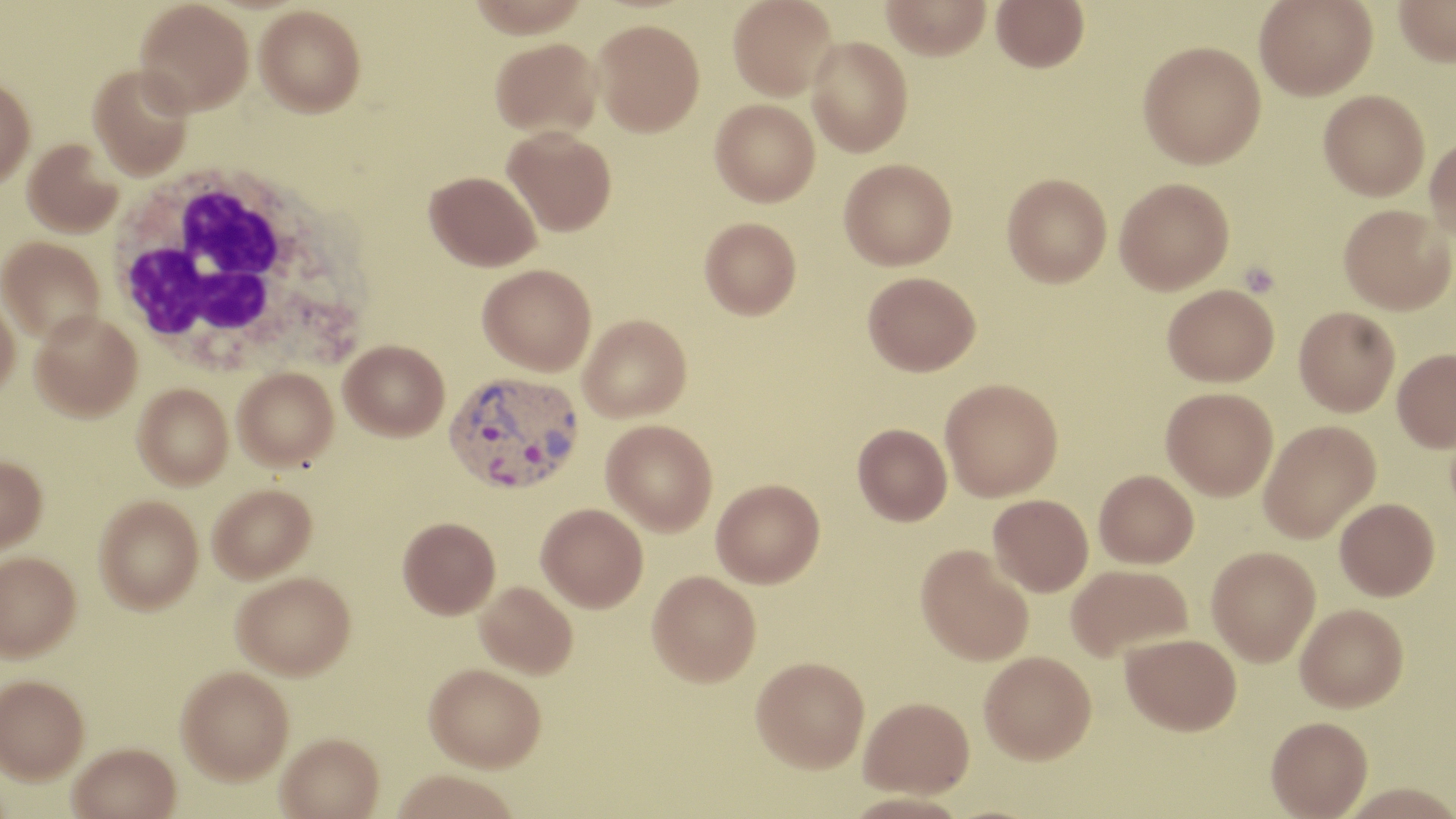
{
  "slide_level_diagnosis": "Plasmodium vivax",
  "white_blood_cell_locations": "approximate bounding boxes as (x1, y1, x2, y2) in pixels: (104, 160, 368, 379)",
  "preparation": "thin blood smear",
  "field_of_view": "single",
  "platelet_locations": "approximate bounding boxes as (x1, y1, x2, y2) in pixels: (1240, 262, 1280, 297)",
  "plasmodium_vivax_infected_red_blood_cell_locations": "approximate bounding boxes as (x1, y1, x2, y2) in pixels: (443, 369, 584, 497)",
  "image_size": "1456×819 pixels",
  "modality": "light microscopy",
  "magnification": "1000x",
  "uninfected_red_blood_cell_locations": "approximate bounding boxes as (x1, y1, x2, y2) in pixels: (134, 0, 254, 116), (728, 0, 838, 100), (881, 0, 991, 60), (991, 0, 1089, 72), (1254, 0, 1377, 100), (1393, 0, 1456, 66), (255, 4, 365, 117), (593, 18, 705, 136), (807, 36, 913, 157), (490, 37, 602, 138), (1138, 41, 1266, 168), (88, 65, 195, 180), (0, 76, 36, 188), (1318, 89, 1429, 200), (710, 98, 820, 206), (502, 127, 616, 235), (1425, 136, 1456, 241), (23, 137, 125, 238), (839, 158, 958, 270), (424, 170, 541, 271), (1002, 173, 1112, 287), (1114, 178, 1234, 294), (1338, 204, 1456, 314), (699, 217, 801, 319), (0, 236, 104, 343), (478, 263, 596, 375), (862, 271, 981, 376), (1162, 283, 1279, 386), (0, 294, 20, 401), (1294, 306, 1400, 415), (30, 312, 142, 421), (578, 314, 691, 423), (339, 339, 449, 441), (1392, 348, 1456, 452), (234, 368, 338, 469), (940, 379, 1063, 500), (133, 383, 232, 488), (1161, 386, 1278, 500), (601, 419, 718, 536), (1258, 420, 1380, 543), (852, 423, 952, 526), (0, 455, 48, 553), (1095, 469, 1198, 568), (711, 480, 825, 590), (208, 484, 317, 584), (988, 494, 1093, 596), (94, 495, 204, 613), (1335, 498, 1440, 601), (536, 504, 648, 614), (398, 517, 501, 620), (915, 545, 1034, 668), (1207, 546, 1320, 666), (0, 551, 80, 661), (1066, 564, 1193, 661), (233, 572, 357, 683), (647, 573, 761, 691), (474, 582, 577, 680), (1296, 603, 1409, 714), (1120, 633, 1242, 737), (979, 653, 1097, 768), (751, 661, 869, 778), (424, 667, 546, 775), (176, 669, 294, 787), (0, 674, 89, 782), (859, 702, 974, 804), (1266, 719, 1373, 819), (277, 736, 384, 819), (69, 745, 180, 819), (391, 773, 519, 819), (1338, 786, 1456, 819)",
  "stain": "May-Grünwald-Giemsa"
}